Comment on the morphology of the erythrocytes.
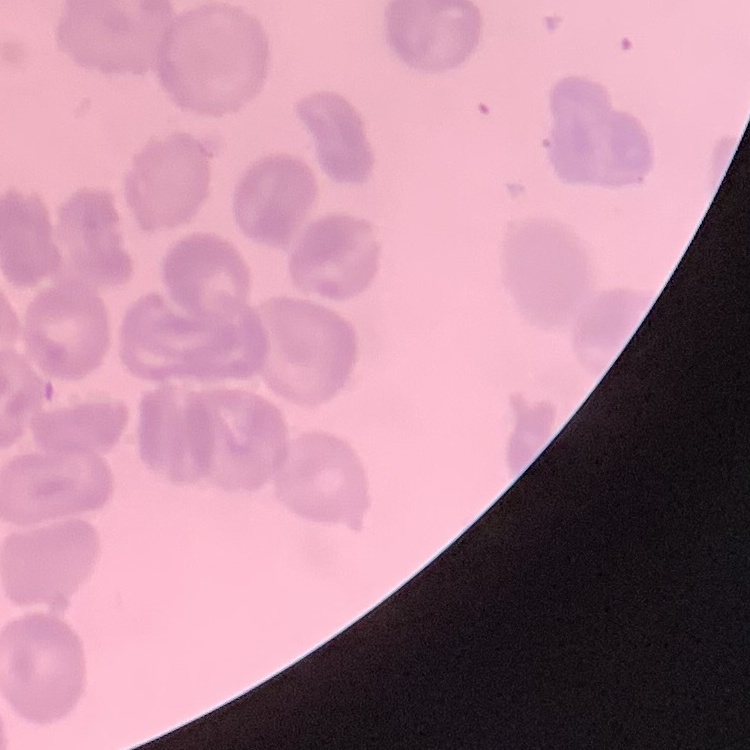

No rouleaux formation.

Summary:
  - Image type: square crop of a larger photomicrograph
  - Preparation: thin blood smear
  - Stain: Field's or Giemsa